Name the parasite shown.
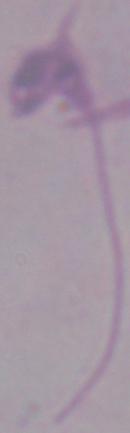
Leishmania.

modality = micrograph
magnification = 1000x